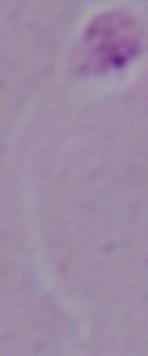

Captured at 1000x magnification. Micrograph. A Leishmania parasite is seen.